Report the malaria status of this cell.
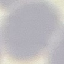

It is uninfected.

capture = smartphone camera at the microscope eyepiece
stain = Giemsa
preparation = thin blood smear
image type = automatically extracted cell patch, resized to 64 × 64 pixels